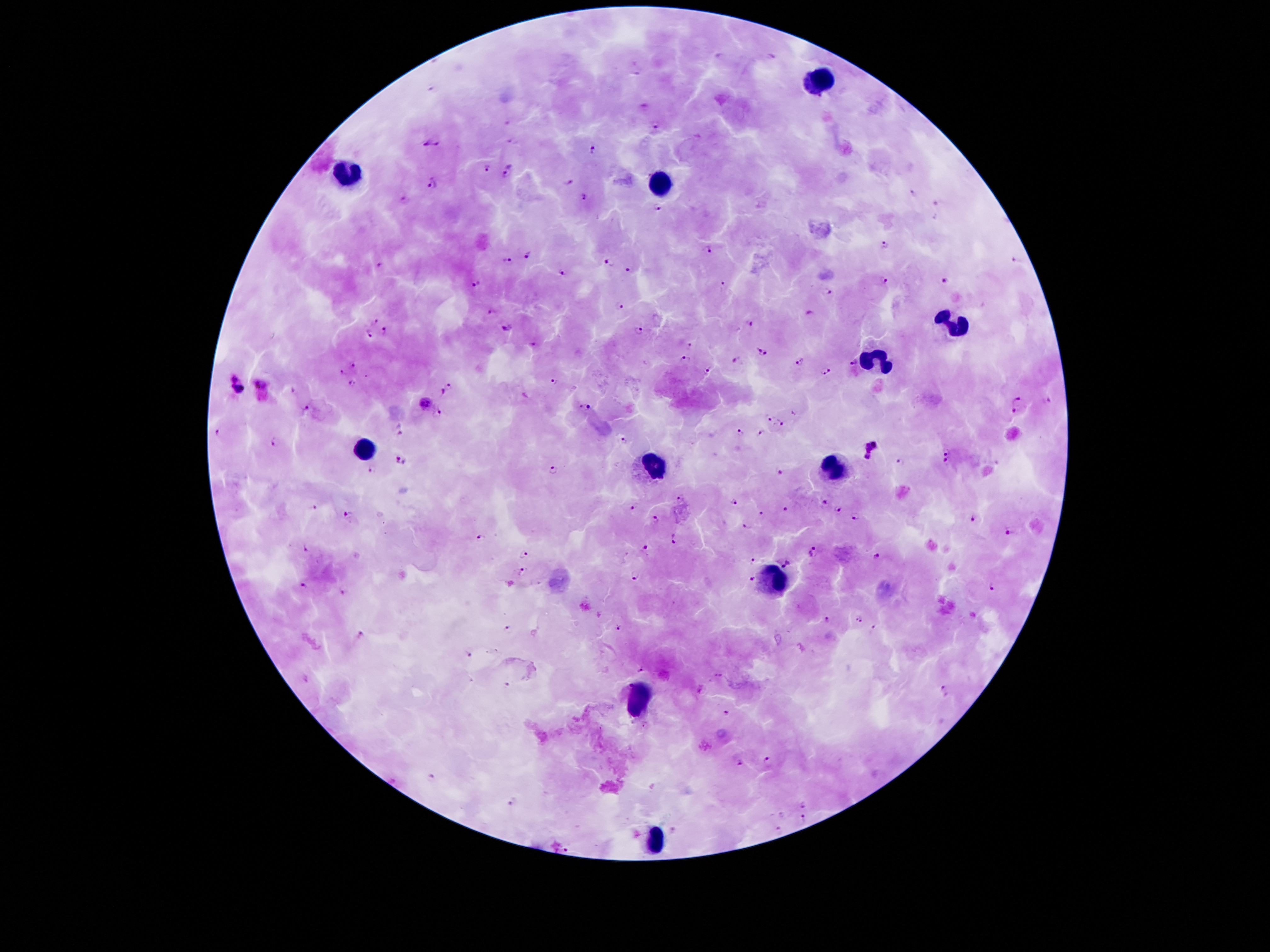
Approximate centers as (x, y) in pixels.
Summary:
  - Malaria parasite locations: (719, 57), (770, 57), (638, 74), (433, 89), (644, 107), (507, 123), (655, 127), (512, 141), (424, 143), (439, 143), (591, 150), (510, 166), (487, 169), (505, 176), (433, 182), (568, 182), (913, 192), (584, 197), (403, 199), (937, 202), (658, 207), (885, 246), (708, 249), (529, 255), (1016, 260), (507, 261), (608, 263), (379, 265), (631, 270), (563, 272), (885, 282), (944, 282), (475, 283), (721, 284), (828, 292), (620, 305), (491, 310), (809, 313), (373, 320), (751, 322), (506, 326), (385, 331), (639, 332), (368, 336), (534, 344), (688, 344), (757, 350), (767, 353), (683, 358), (734, 360), (799, 362), (854, 363), (354, 365), (709, 369), (826, 371), (340, 373), (236, 377), (553, 380), (353, 382), (261, 383), (449, 385), (292, 389), (239, 390), (442, 392), (1018, 398), (1047, 400), (426, 402), (585, 407), (306, 408), (1014, 410), (437, 414), (769, 419), (782, 422), (399, 429), (739, 432), (218, 433), (762, 434), (623, 441), (274, 442), (947, 449), (874, 450), (401, 461), (945, 461), (900, 462), (371, 469), (553, 469), (781, 472), (680, 499), (733, 502), (823, 502), (633, 506), (313, 507), (787, 509), (838, 509), (347, 513), (761, 514), (855, 517), (973, 518), (655, 520), (746, 526), (1011, 532), (481, 537), (674, 540), (306, 547), (644, 548), (813, 551), (523, 553), (877, 555), (751, 559), (786, 562), (523, 571), (636, 576), (754, 578), (303, 585), (994, 588), (343, 593), (859, 619), (827, 620), (873, 626), (618, 627), (508, 629), (361, 636), (469, 655), (642, 671), (718, 675), (306, 679), (507, 685), (944, 690), (727, 711), (644, 724), (769, 761), (738, 763), (431, 776), (513, 802), (805, 805), (805, 816), (779, 828), (566, 850)
  - Leukocyte locations: (820, 83), (346, 174), (663, 184), (953, 324), (876, 361), (367, 448), (656, 466), (834, 469), (776, 580), (640, 697), (657, 840)
  - Capture: smartphone through the microscope eyepiece
  - Image size: 1270×952 pixels
  - Patient malaria status: positive for Plasmodium falciparum
  - Preparation: thick blood smear
  - Stain: Giemsa
  - Magnification: 100x
  - Field of view: one from this slide